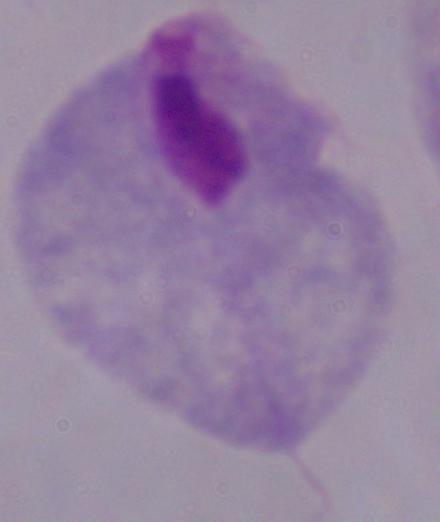

Summary:
  - Magnification: 1000x
  - Modality: photomicrograph
  - Identification: trichomonad